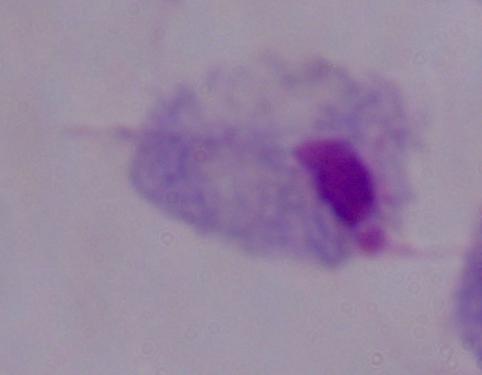

magnification = 1000x
modality = micrograph
identification = trichomonad